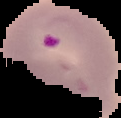

From a thin blood film. Image is 121×118 pixels. Result: malaria parasites detected. The area outside the segmented cell region is set to black.